Report the malaria status.
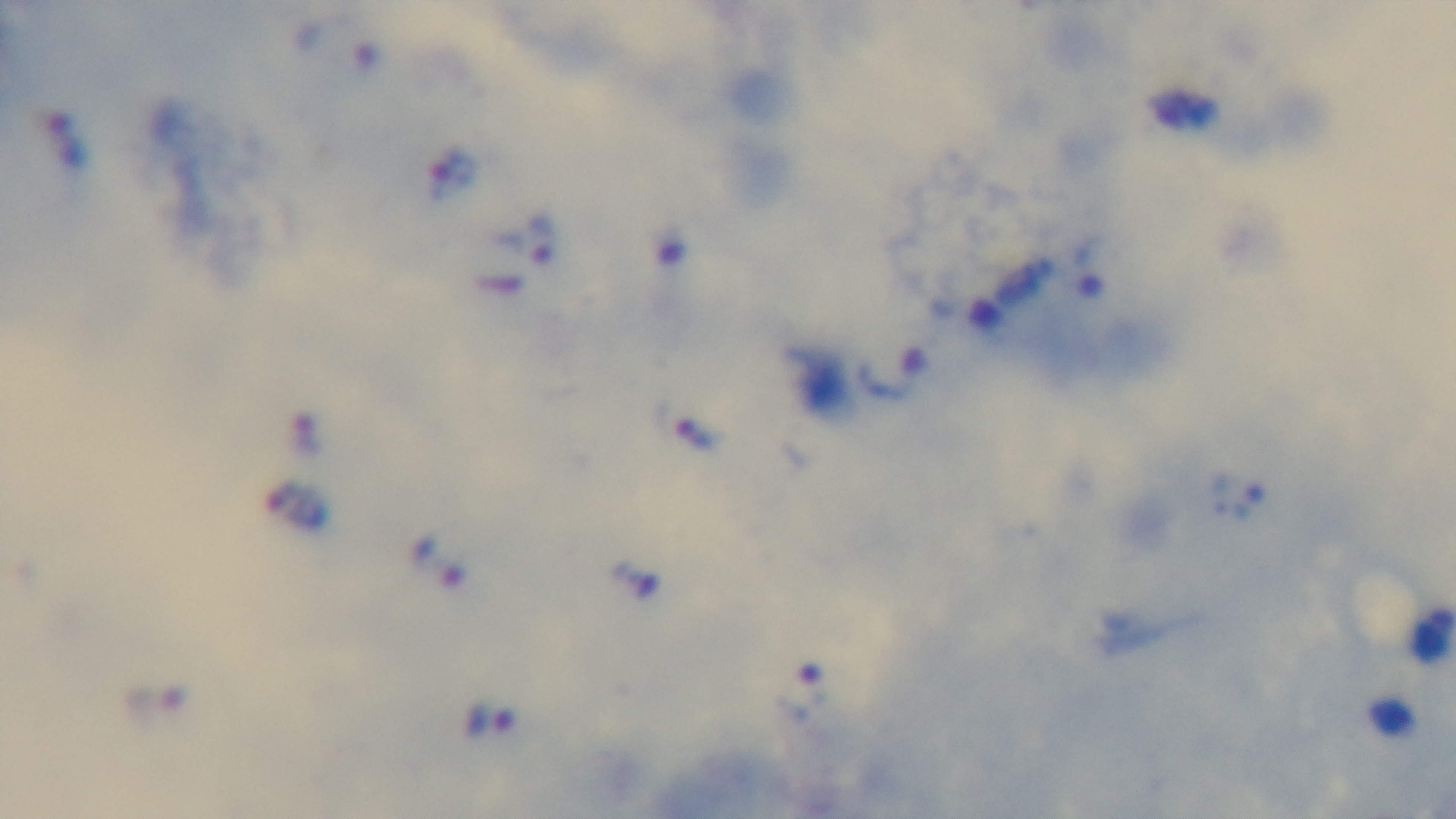

Positive.

capture = mounted 4K digital camera
modality = light microscopy
preparation = thick
stain = Giemsa
field of view = single
objective = 100x oil immersion